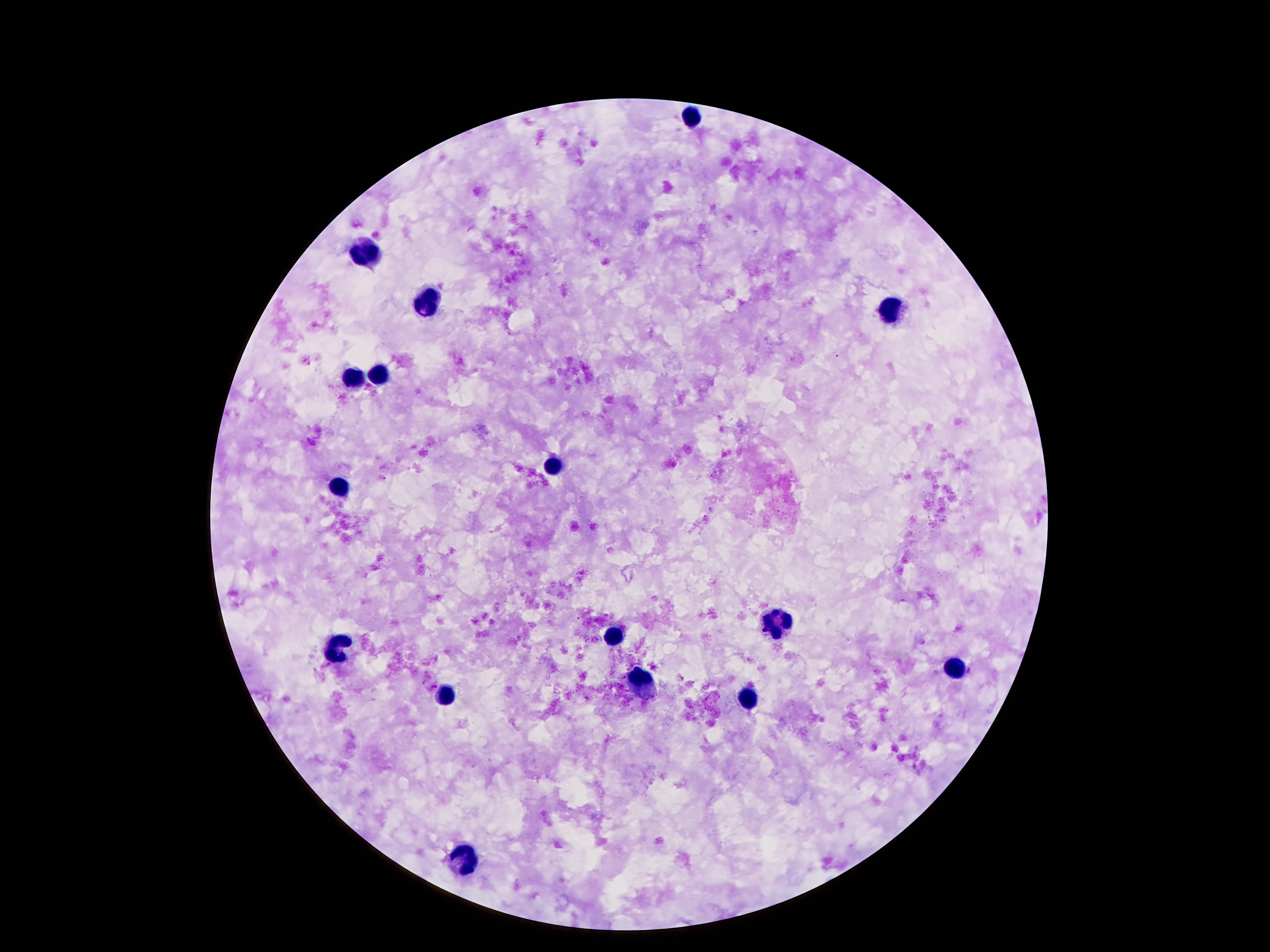 Approximate centers as [x, y] in pixels. Leukocyte locations: [692, 115], [365, 253], [425, 300], [894, 309], [378, 374], [350, 378], [550, 469], [339, 489], [778, 623], [612, 637], [333, 646], [955, 665], [643, 682], [447, 695], [746, 697], [470, 858]. 100x magnification. Photographed through the microscope eyepiece with a smartphone camera. Giemsa-stained preparation. Image is 1270×952 pixels. Thick blood film. One field from this slide. Patient malaria status: negative.